Locate every Plasmodium falciparum parasite and give its life-cycle stage, and locate every leukocyte and any debris.
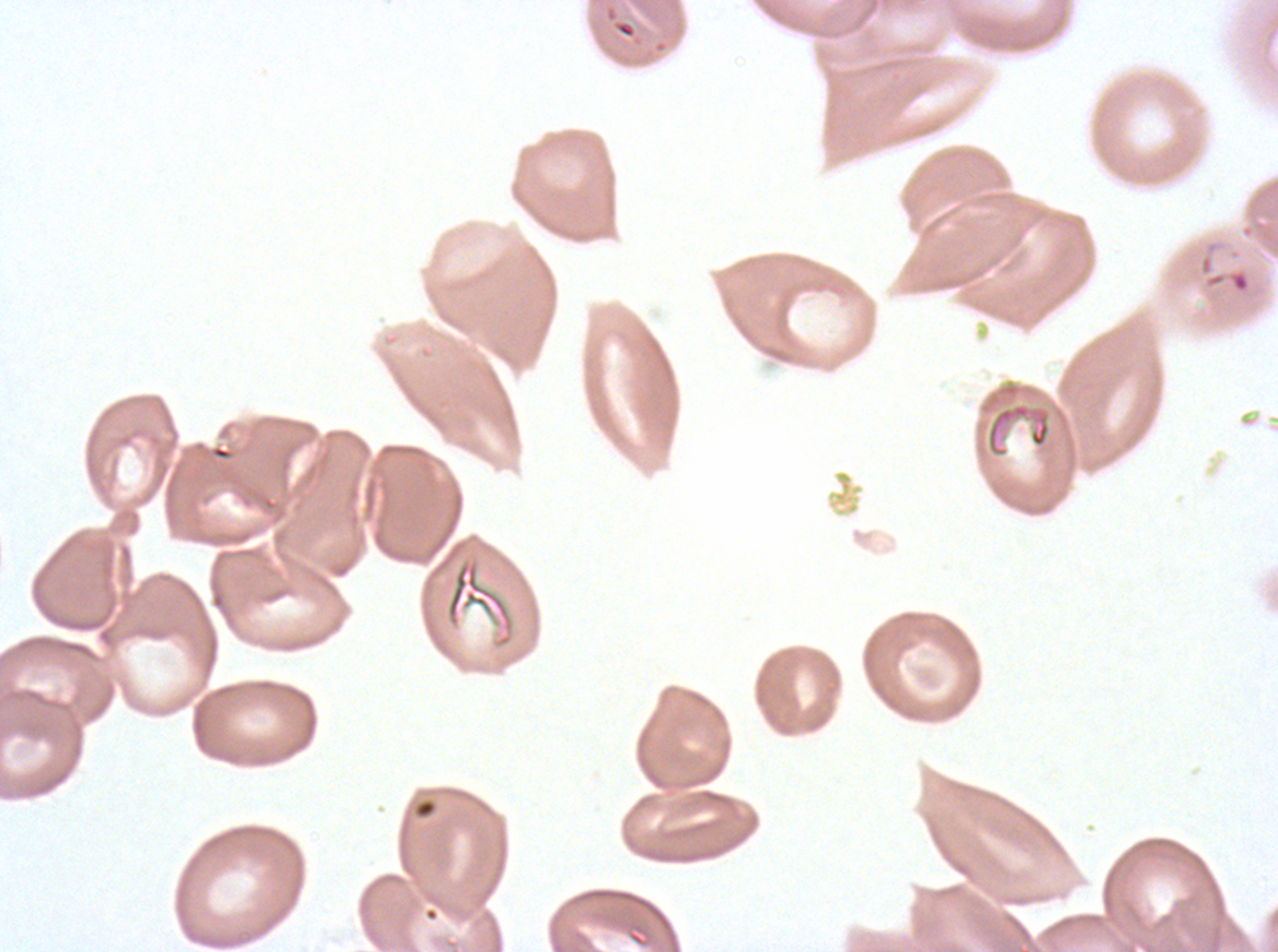

Approximate bounding boxes as (x1, y1, x2, y2) in pixels.
Rings: (1198, 253, 1252, 295).
Debris: (445, 557, 515, 649).
No late-ring/early-trophozoite forms, mid trophozoites, late trophozoites, early schizonts, late schizonts, segmenters, gametocytes, or leukocytes observed.

image size = 1278×952 pixels
preparation = thin blood smear
specimen = ex-vivo Plasmodium falciparum culture from a patient in The Gambia, grown for 24 to 48 hours
stain = Giemsa
field of view = one sub-image of a larger composite